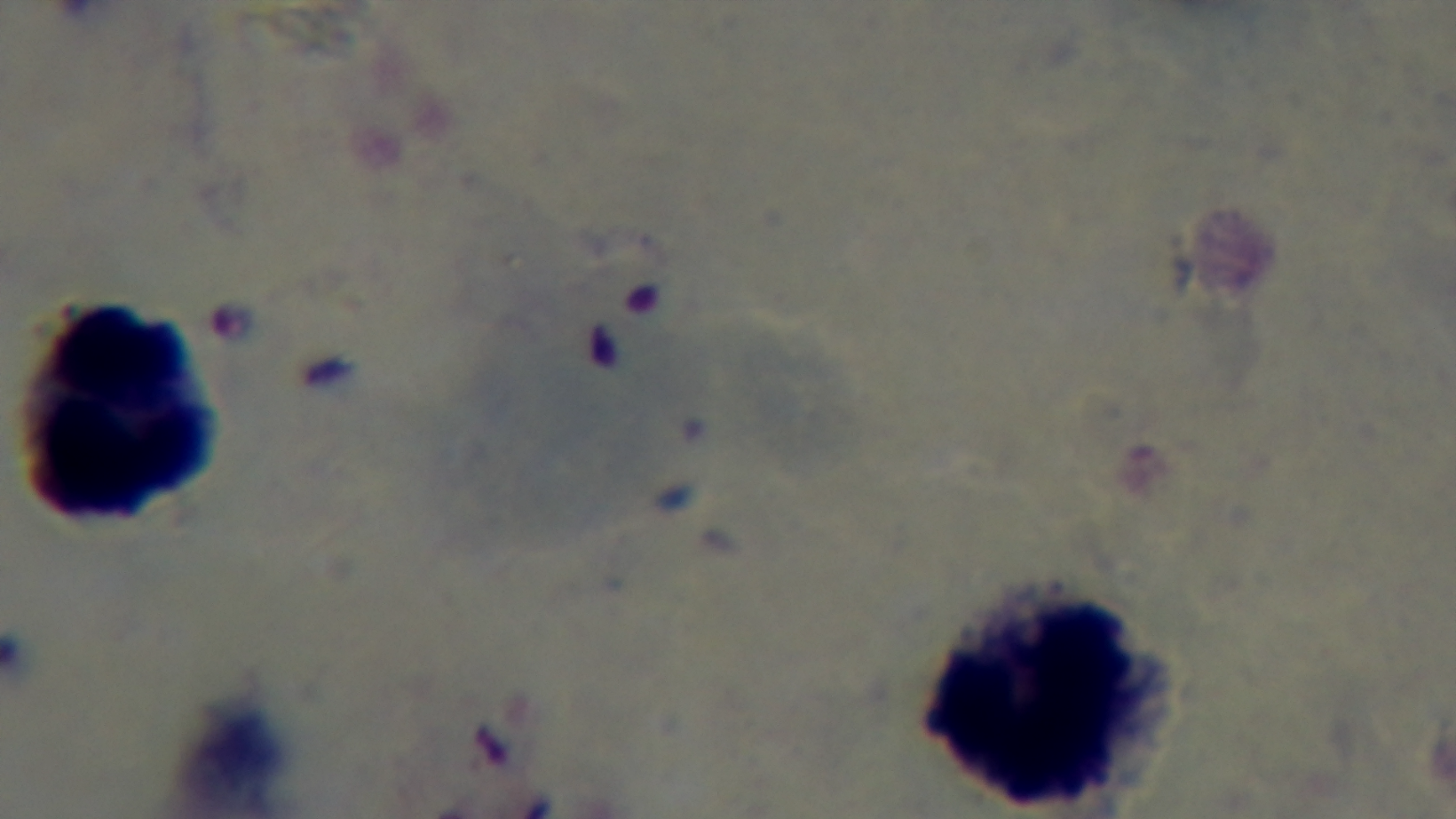
Summary:
  - Preparation: thick smear
  - Malaria status: positive
  - Modality: light microscopy
  - Stain: Giemsa
  - Capture: mounted 4K digital camera
  - Objective: 100x oil immersion
  - Field of view: single